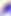

Summary:
  - Identification: Toxoplasma gondii
  - Modality: photomicrograph
  - Magnification: 400x